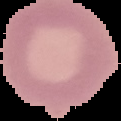

Result: no Plasmodium parasites detected. Cell region segmented out of the field of view; the surrounding area is masked to black. Image is 121×121 pixels. From a thin blood smear.